Report the malaria status of this cell.
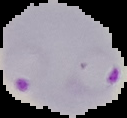

It is parasitized.

Image is 127×118 pixels. From a thin blood smear. Segmented cell region on a black background.